Describe the morphology of the erythrocytes.
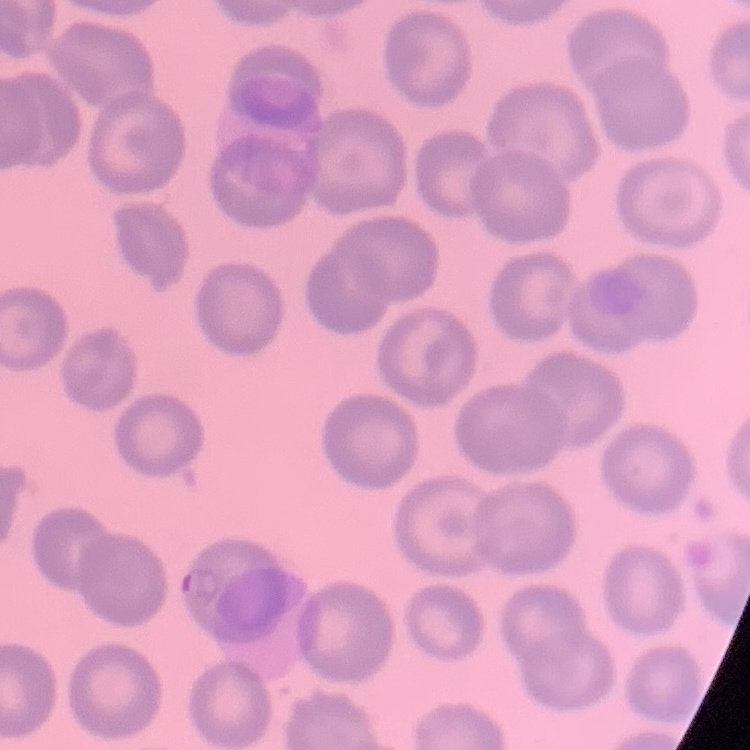
No rouleaux formation.

image type = one tile cut from a larger photomicrograph
preparation = thin blood smear
stain = Field's or Giemsa